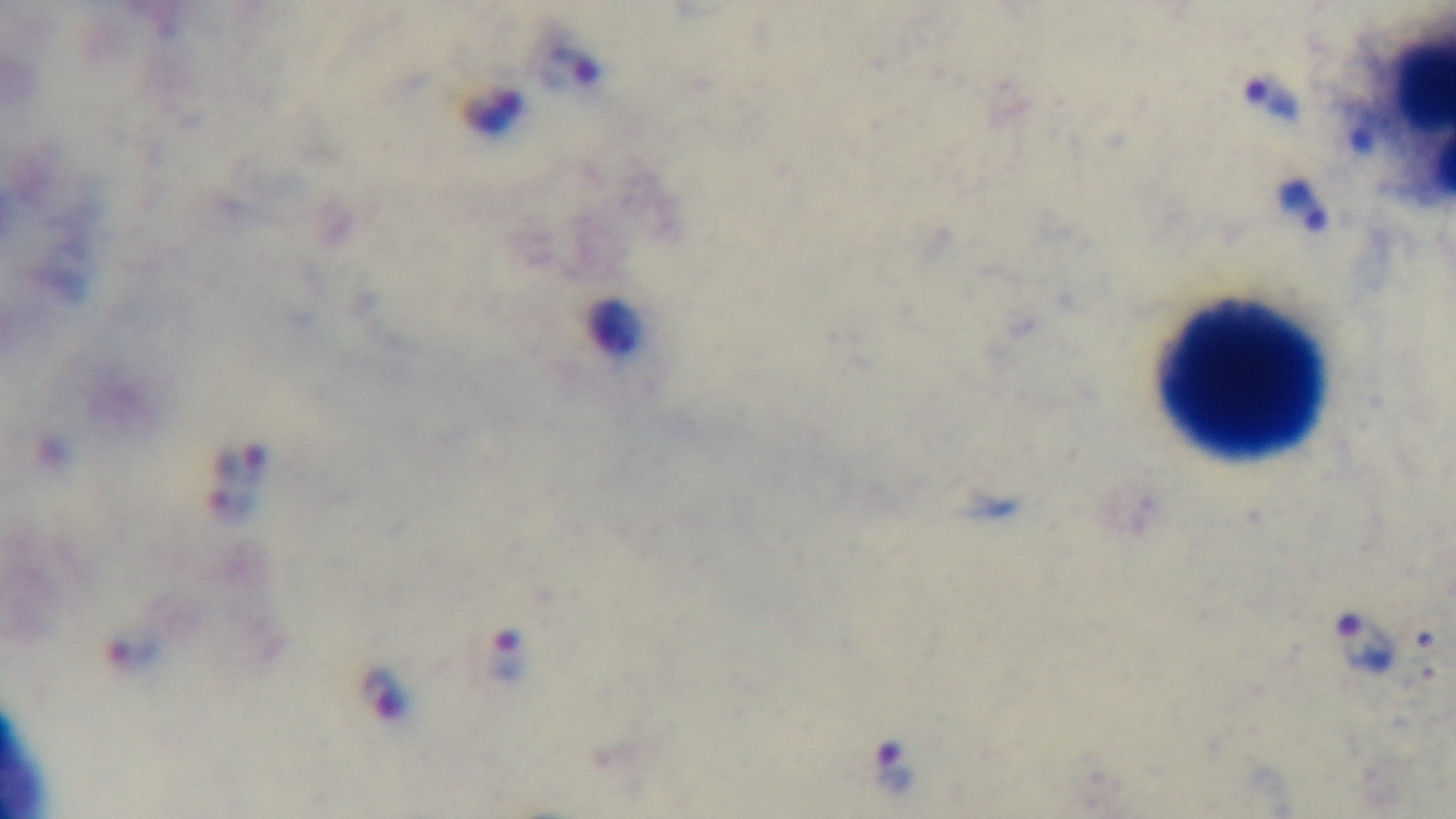
Summary:
  - Modality: light microscopy
  - Field of view: single
  - Capture: mounted 4K digital camera
  - Objective: 100x oil immersion
  - Stain: Giemsa
  - Malaria status: infected
  - Preparation: thick smear